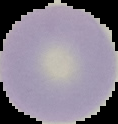
{
  "preparation": "thin blood film",
  "malaria_status": "uninfected",
  "image_type": "segmented cell region with the area outside set to black",
  "image_size": "118×124 pixels"
}